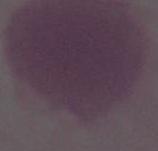 Micrograph. An erythrocyte is seen. Captured at 1000x magnification.